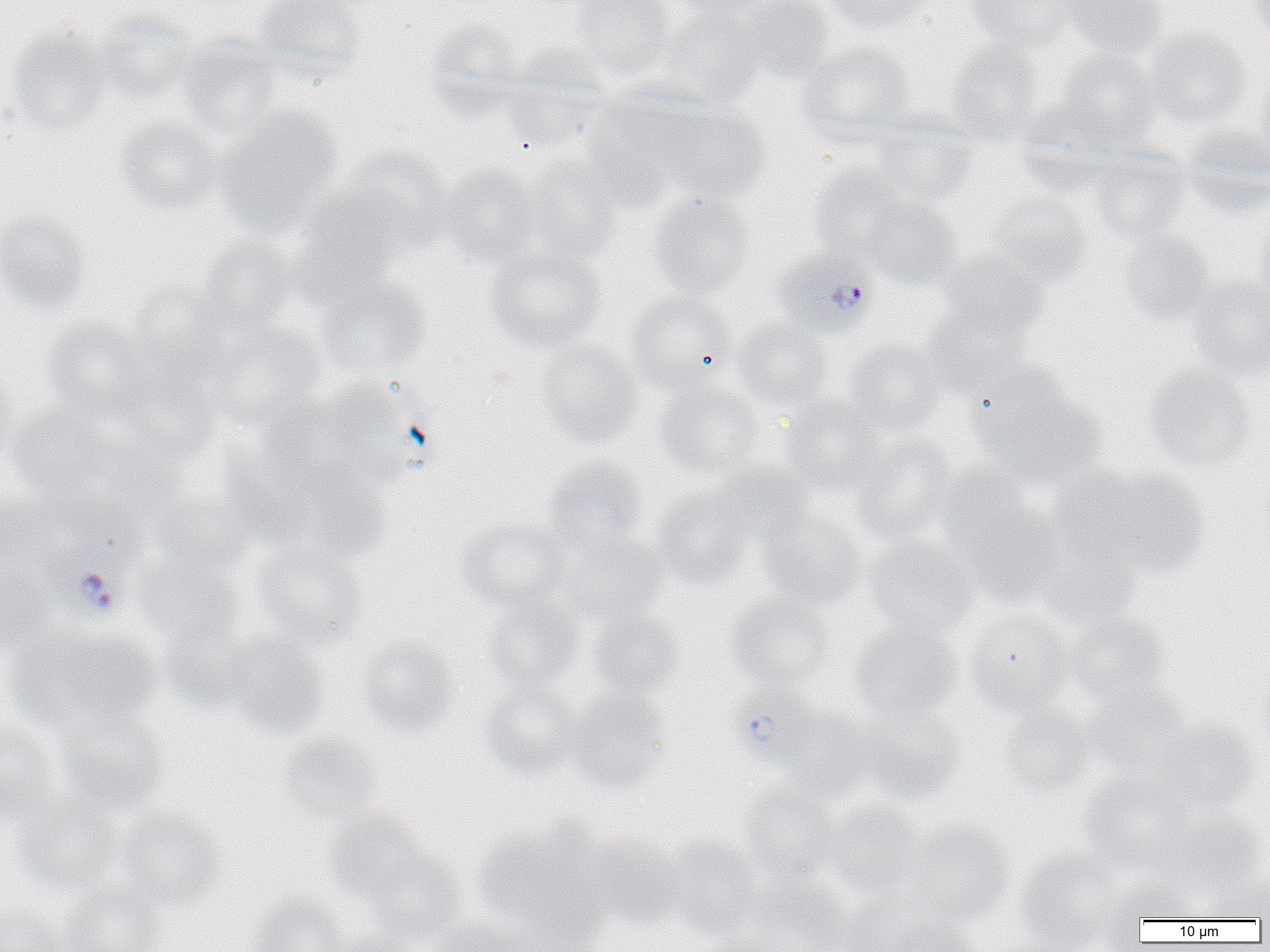
Summary:
  - Coordinate format: approximate bounding boxes as (x1,y1)-(x2,y2) corner pairs in pixels
  - Uninfected red blood cell locations: (252,0)-(367,81), (572,0)-(675,77), (662,0)-(777,20), (823,0)-(937,34), (963,0)-(1076,53), (1051,0)-(1169,60), (1248,0)-(1270,46), (734,1)-(834,83), (658,8)-(767,107), (92,13)-(197,107), (425,20)-(526,122), (6,29)-(114,137), (1142,29)-(1253,131), (177,36)-(288,139), (944,41)-(1048,145), (796,42)-(917,142), (501,46)-(615,150), (1050,52)-(1161,154), (1251,64)-(1270,172), (648,101)-(771,204), (211,107)-(343,237), (581,107)-(684,213), (113,117)-(224,218), (870,122)-(979,210), (1180,128)-(1270,218), (1085,148)-(1192,245), (338,149)-(455,257), (521,157)-(624,263), (810,165)-(915,262), (439,166)-(543,268), (290,187)-(408,300), (646,192)-(757,301), (983,194)-(1092,289), (857,196)-(962,291), (0,208)-(92,317), (1253,212)-(1270,321), (1114,228)-(1214,326), (195,236)-(300,340), (484,246)-(605,354), (936,249)-(1049,343), (317,276)-(432,381), (1186,277)-(1270,380), (128,280)-(237,383), (623,292)-(738,394), (922,310)-(1032,400), (40,318)-(152,420), (731,320)-(836,416), (207,323)-(328,429), (534,339)-(644,450), (843,340)-(947,438), (113,361)-(224,465), (1142,364)-(1257,474), (0,367)-(19,475), (971,373)-(1106,491), (272,381)-(418,497), (654,382)-(767,481), (779,398)-(885,496), (7,402)-(125,501), (849,438)-(960,547), (235,448)-(390,565), (544,459)-(650,556), (711,463)-(815,547), (932,463)-(1040,570), (1063,466)-(1210,583), (653,486)-(757,589), (147,490)-(256,578), (948,492)-(1066,608), (0,495)-(58,568), (760,514)-(868,614), (456,521)-(570,614), (555,534)-(667,627), (1033,535)-(1143,629), (864,537)-(982,643), (253,542)-(371,651), (0,558)-(55,655), (134,558)-(245,650), (483,593)-(589,695), (726,595)-(836,691), (964,610)-(1077,717), (586,611)-(685,701), (1066,613)-(1168,707), (848,622)-(965,723), (11,623)-(164,738), (159,625)-(263,719), (219,632)-(329,740), (356,637)-(462,738), (1254,665)-(1270,757), (480,680)-(583,781), (1086,687)-(1194,779), (563,690)-(670,794), (999,702)-(1098,798), (855,706)-(965,805), (775,709)-(875,803), (57,710)-(170,821), (0,714)-(65,826), (1154,722)-(1260,816), (275,733)-(382,830), (1076,770)-(1196,874), (738,785)-(843,885), (11,793)-(126,897), (820,798)-(929,902), (113,807)-(228,913), (1168,809)-(1267,896), (324,812)-(434,909), (473,821)-(608,940), (900,821)-(1017,928), (586,837)-(690,932), (664,837)-(766,942), (363,844)-(468,942), (1014,849)-(1126,951), (1105,874)-(1206,924), (1198,875)-(1270,921), (734,878)-(853,952), (56,879)-(168,952), (250,895)-(353,952), (841,899)-(974,952), (0,910)-(67,952), (428,918)-(531,952), (705,930)-(804,952)
  - Plasmodium falciparum-infected red blood cell locations: (770,251)-(880,340), (42,504)-(145,622), (732,694)-(862,760)
  - Slide-level diagnosis: Plasmodium falciparum
  - Image size: 1270×952 pixels
  - Magnification: 1000x
  - Field of view: single
  - Preparation: thin blood smear
  - Modality: optical microscopy